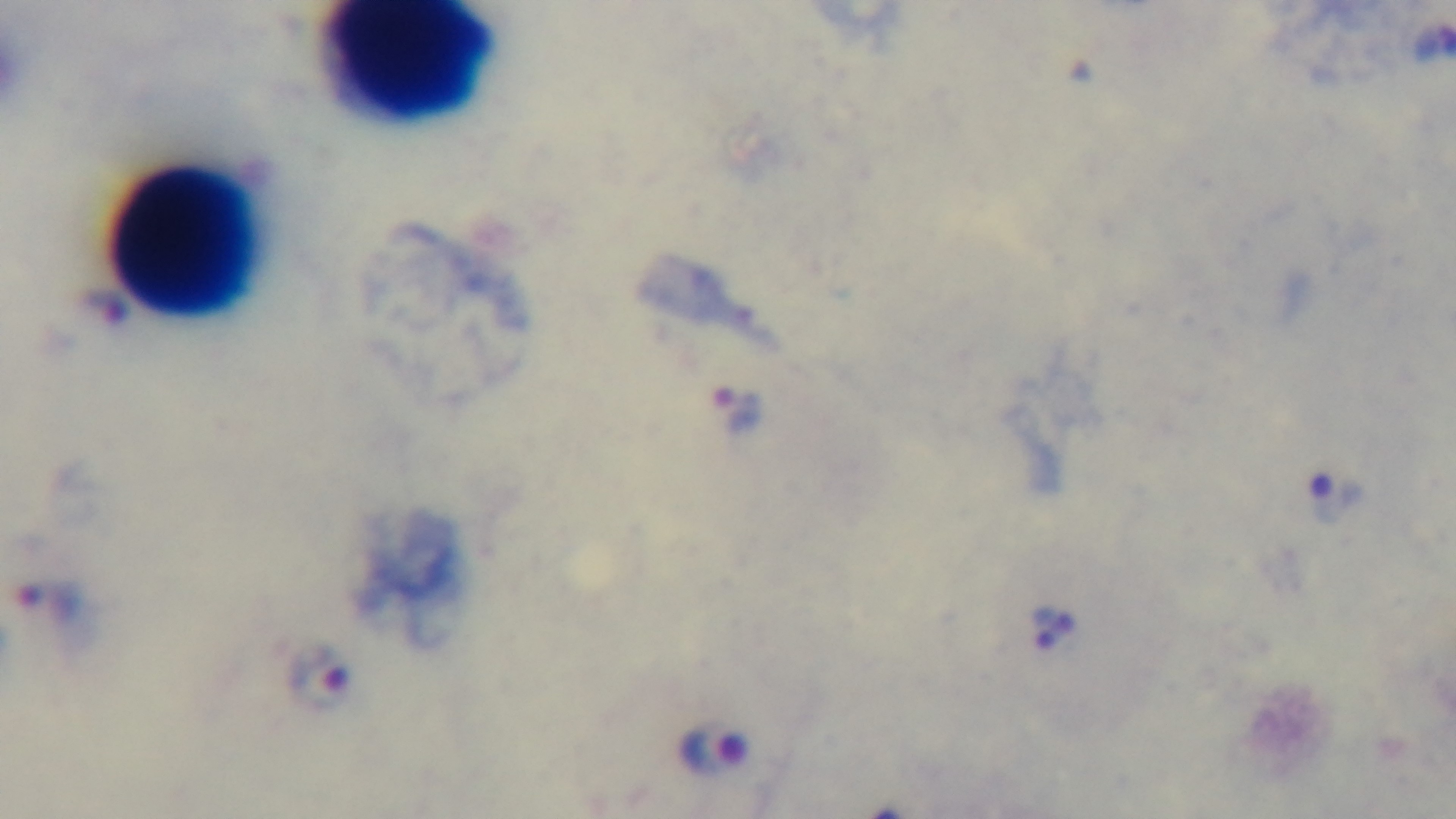
Oil-immersion objective, 100x. Malaria status: infected. Preparation: thick smear. Giemsa stain. Light microscopy. Mounted 4K digital camera. One field from the slide.